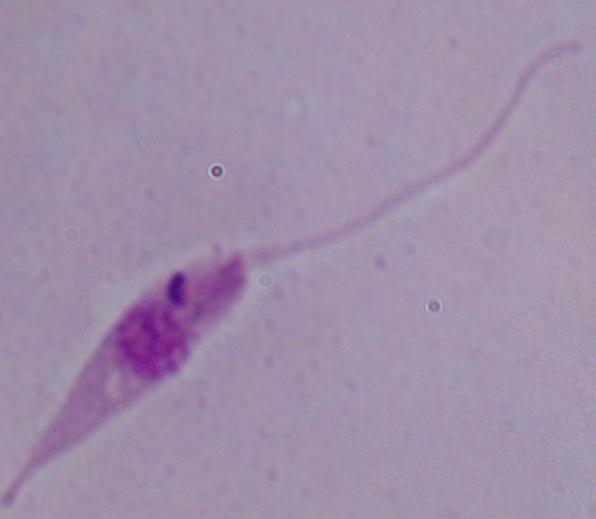
A Leishmania parasite is seen. Micrograph. Captured at 1000x magnification.